Give the position of every leukocyte visible.
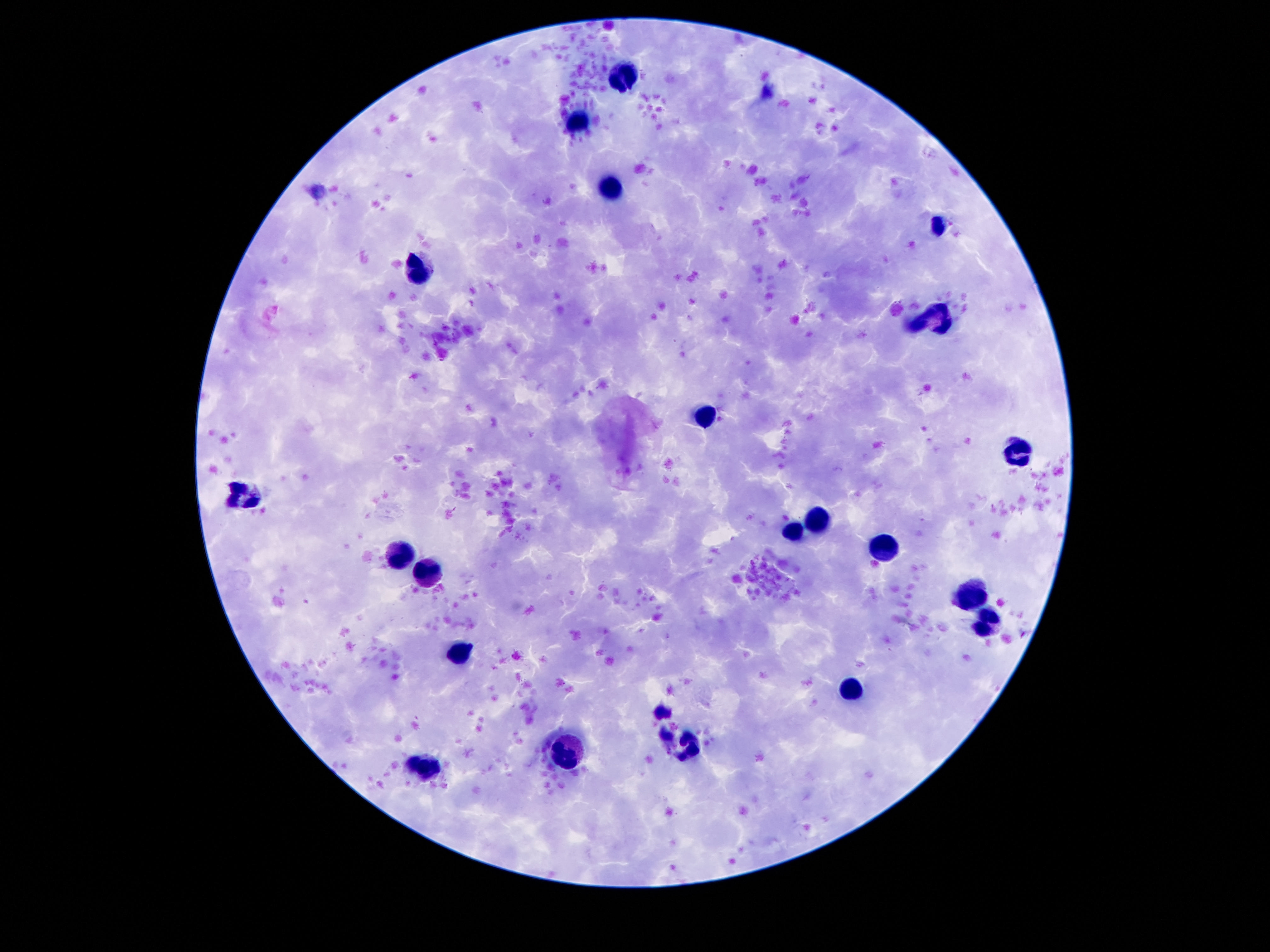
Approximate object centers, in pixels from the top-left corner.
Leukocytes: (x=621, y=74), (x=575, y=124), (x=609, y=188), (x=934, y=224), (x=416, y=274), (x=943, y=315), (x=907, y=324), (x=709, y=417), (x=1020, y=451), (x=241, y=496), (x=818, y=517), (x=793, y=533), (x=884, y=548), (x=400, y=555), (x=425, y=576), (x=968, y=594), (x=988, y=621), (x=462, y=653), (x=855, y=687), (x=691, y=746), (x=568, y=750), (x=423, y=764).

capture: smartphone camera through the microscope eyepiece
magnification: 100x
field_of_view: single
image_size: 1270×952 pixels
stain: Giemsa
preparation: thick blood film
patient_malaria_status: uninfected